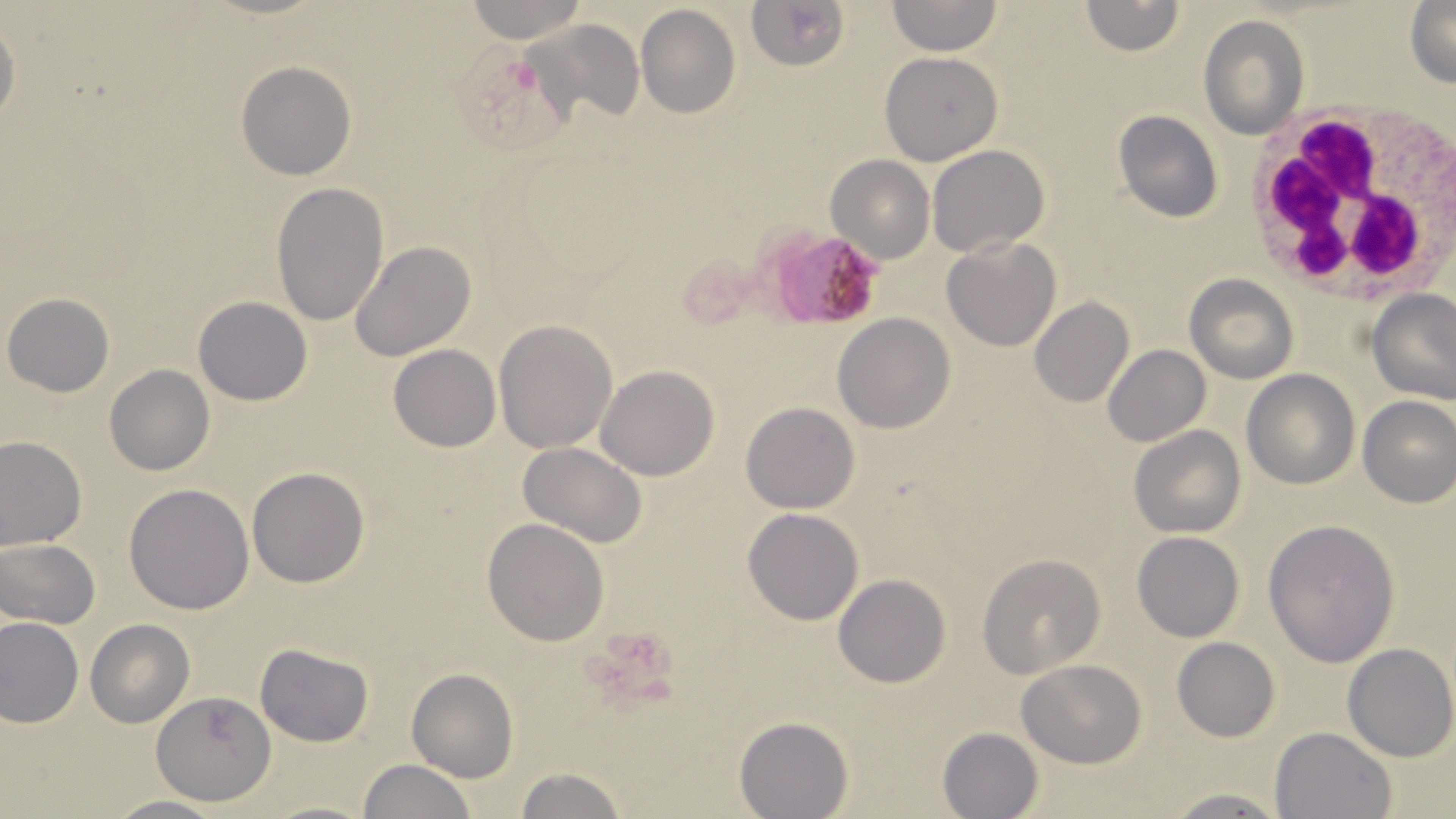
slide-level diagnosis = Plasmodium falciparum
uninfected red blood cell locations = approximate bounding boxes as (x1, y1, x2, y2) in pixels: (464, 0, 587, 43), (747, 0, 851, 70), (888, 0, 1000, 55), (1079, 0, 1183, 56), (1406, 1, 1456, 90), (635, 5, 740, 118), (0, 15, 21, 131), (1198, 15, 1309, 139), (529, 17, 645, 128), (879, 51, 1002, 165), (235, 61, 357, 181), (1114, 109, 1223, 222), (928, 144, 1050, 258), (826, 155, 934, 265), (272, 182, 389, 327), (941, 238, 1062, 352), (349, 241, 476, 362), (1184, 273, 1299, 383), (1369, 289, 1456, 404), (3, 291, 115, 397), (192, 296, 313, 406), (1027, 296, 1134, 408), (832, 312, 956, 434), (493, 320, 617, 452), (388, 344, 501, 452), (1103, 345, 1210, 446), (105, 364, 215, 476), (596, 365, 720, 481), (1242, 368, 1361, 490), (1356, 394, 1456, 507), (740, 402, 860, 514), (1129, 424, 1246, 538), (0, 436, 86, 551), (519, 442, 647, 549), (247, 466, 371, 588), (124, 483, 255, 614), (742, 507, 864, 625), (482, 518, 610, 646), (1263, 520, 1399, 667), (1132, 532, 1244, 643), (1, 539, 100, 631), (978, 554, 1104, 679), (833, 574, 951, 688), (1, 616, 84, 728), (85, 618, 195, 728), (1171, 637, 1280, 742), (254, 642, 376, 747), (1342, 642, 1456, 762), (1017, 659, 1148, 768), (406, 668, 518, 784), (152, 692, 275, 804), (734, 716, 853, 818), (1269, 726, 1397, 819), (936, 727, 1043, 819), (357, 758, 476, 819), (511, 767, 630, 819), (1160, 788, 1294, 817), (103, 795, 226, 818), (264, 799, 377, 819)
magnification = 1000x
Plasmodium falciparum-infected red blood cell locations = approximate bounding boxes as (x1, y1, x2, y2) in pixels: (762, 224, 883, 331)
white blood cell locations = approximate bounding boxes as (x1, y1, x2, y2) in pixels: (1241, 104, 1456, 307)
image size = 1456×819 pixels
preparation = thin blood smear
stain = May-Grünwald-Giemsa
field of view = one of a larger specimen
modality = light microscopy